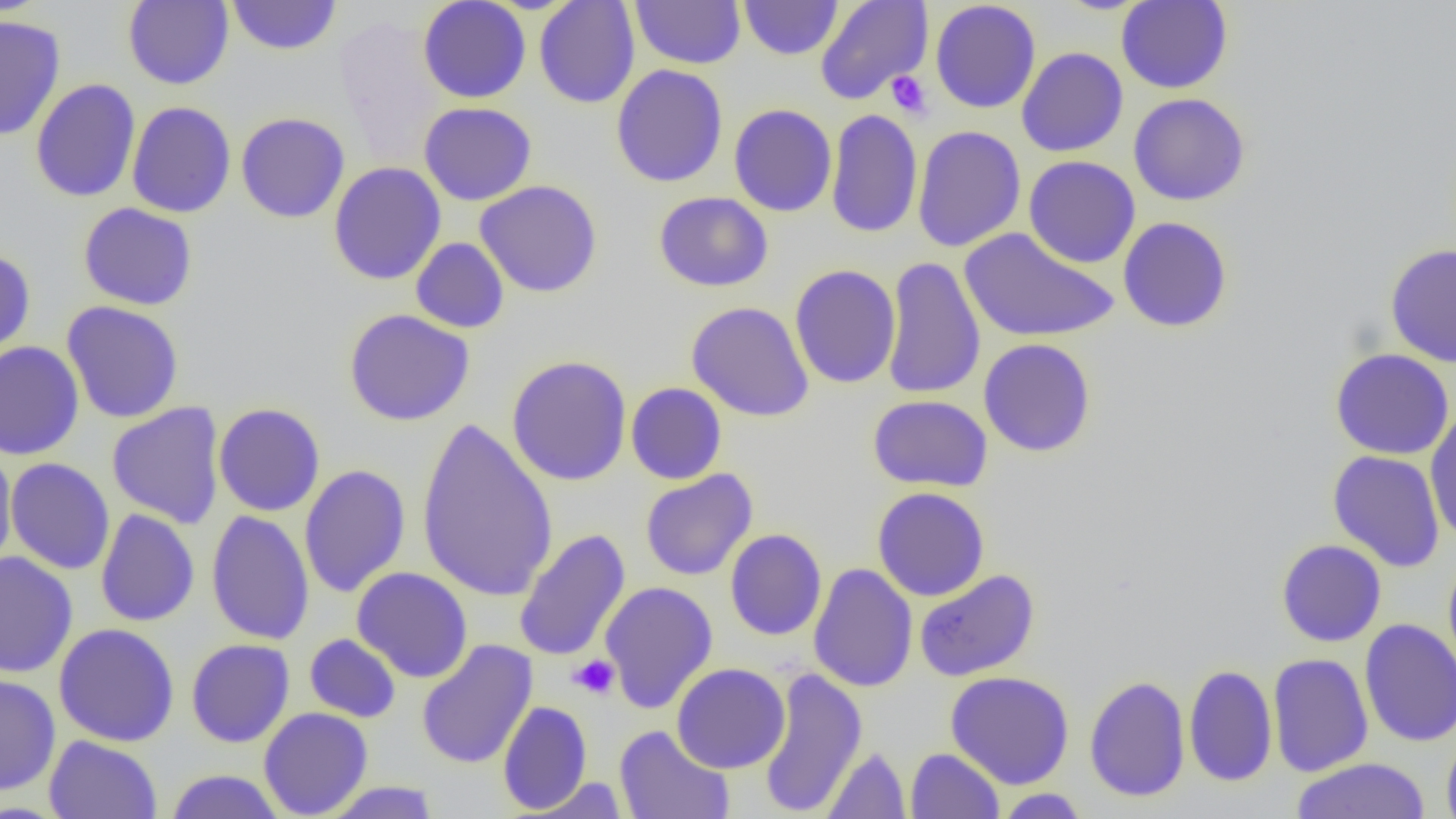
Approximate bounding boxes as named x1/y1/x2/y2 corners in pixels. Uninfected red blood cell locations: (x1=123, y1=0, x2=234, y2=90), (x1=227, y1=0, x2=341, y2=56), (x1=418, y1=0, x2=531, y2=103), (x1=534, y1=0, x2=640, y2=109), (x1=630, y1=0, x2=746, y2=69), (x1=815, y1=0, x2=933, y2=105), (x1=930, y1=0, x2=1041, y2=113), (x1=1116, y1=0, x2=1233, y2=93), (x1=738, y1=1, x2=843, y2=60), (x1=0, y1=14, x2=66, y2=141), (x1=1017, y1=47, x2=1128, y2=157), (x1=611, y1=64, x2=728, y2=188), (x1=30, y1=78, x2=140, y2=203), (x1=1129, y1=93, x2=1250, y2=206), (x1=126, y1=101, x2=236, y2=218), (x1=419, y1=102, x2=537, y2=206), (x1=728, y1=103, x2=837, y2=217), (x1=825, y1=108, x2=923, y2=239), (x1=235, y1=112, x2=350, y2=223), (x1=912, y1=125, x2=1026, y2=252), (x1=1024, y1=155, x2=1140, y2=268), (x1=328, y1=162, x2=446, y2=285), (x1=475, y1=180, x2=603, y2=298), (x1=653, y1=191, x2=773, y2=292), (x1=78, y1=203, x2=198, y2=310), (x1=1117, y1=216, x2=1233, y2=333), (x1=960, y1=227, x2=1119, y2=343), (x1=411, y1=237, x2=509, y2=333), (x1=1385, y1=243, x2=1456, y2=368), (x1=0, y1=247, x2=36, y2=361), (x1=881, y1=256, x2=986, y2=400), (x1=789, y1=265, x2=901, y2=389), (x1=61, y1=301, x2=184, y2=423), (x1=686, y1=301, x2=815, y2=422), (x1=344, y1=308, x2=475, y2=426), (x1=977, y1=338, x2=1096, y2=458), (x1=0, y1=340, x2=85, y2=461), (x1=1330, y1=348, x2=1455, y2=460), (x1=506, y1=355, x2=632, y2=486), (x1=625, y1=382, x2=727, y2=484), (x1=867, y1=395, x2=993, y2=492), (x1=107, y1=402, x2=226, y2=529), (x1=213, y1=402, x2=325, y2=516), (x1=1424, y1=406, x2=1456, y2=546), (x1=416, y1=417, x2=558, y2=603), (x1=0, y1=446, x2=17, y2=573), (x1=1328, y1=450, x2=1445, y2=572), (x1=4, y1=458, x2=115, y2=575), (x1=299, y1=464, x2=411, y2=598), (x1=640, y1=469, x2=757, y2=581), (x1=871, y1=486, x2=990, y2=601), (x1=95, y1=508, x2=200, y2=627), (x1=206, y1=509, x2=314, y2=645), (x1=514, y1=528, x2=631, y2=662), (x1=725, y1=528, x2=827, y2=641), (x1=1276, y1=539, x2=1387, y2=647), (x1=0, y1=551, x2=78, y2=679), (x1=1443, y1=555, x2=1456, y2=676), (x1=808, y1=563, x2=918, y2=692), (x1=352, y1=567, x2=473, y2=683), (x1=913, y1=569, x2=1040, y2=682), (x1=600, y1=581, x2=718, y2=714), (x1=1359, y1=619, x2=1456, y2=747), (x1=53, y1=622, x2=180, y2=747), (x1=304, y1=633, x2=402, y2=723), (x1=186, y1=639, x2=295, y2=747), (x1=416, y1=640, x2=538, y2=769), (x1=1268, y1=652, x2=1373, y2=777), (x1=672, y1=663, x2=790, y2=773), (x1=1183, y1=664, x2=1278, y2=787), (x1=757, y1=668, x2=867, y2=818), (x1=946, y1=670, x2=1075, y2=789), (x1=0, y1=673, x2=61, y2=796), (x1=1083, y1=675, x2=1191, y2=802), (x1=497, y1=700, x2=592, y2=814), (x1=259, y1=708, x2=373, y2=818), (x1=614, y1=725, x2=735, y2=819), (x1=1442, y1=731, x2=1456, y2=819), (x1=44, y1=735, x2=162, y2=818), (x1=822, y1=746, x2=911, y2=818), (x1=905, y1=748, x2=1004, y2=818), (x1=1290, y1=757, x2=1430, y2=819), (x1=165, y1=769, x2=285, y2=819), (x1=524, y1=777, x2=630, y2=818), (x1=319, y1=781, x2=442, y2=818), (x1=993, y1=788, x2=1091, y2=817). Platelet locations: (x1=885, y1=70, x2=933, y2=120), (x1=568, y1=654, x2=620, y2=699). Slide-level diagnosis: negative for blood parasites. One field of a larger specimen. Light microscopy. 1000x magnification. Thin blood smear. Image is 1456×819 pixels.